Give the position of every leukocyte visible.
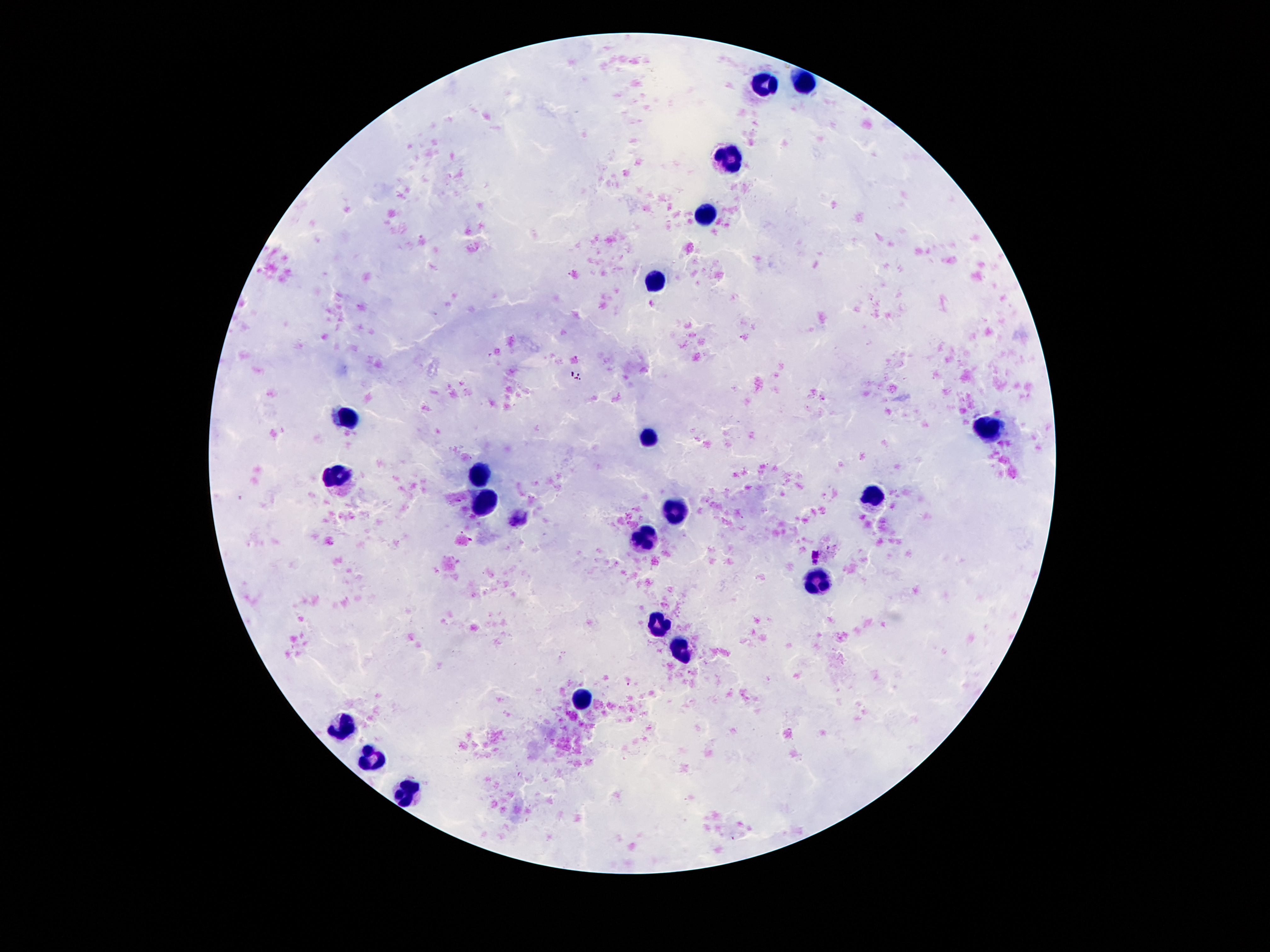
Approximate centers as (x, y) in pixels.
Leukocytes: (805, 81), (761, 87), (727, 159), (705, 215), (657, 279), (349, 417), (990, 430), (650, 439), (480, 472), (336, 476), (873, 495), (486, 503), (674, 515), (645, 539), (816, 581), (657, 625), (685, 652), (584, 696), (343, 725), (369, 760), (407, 793).

field_of_view: one from this slide
magnification: 100x
stain: Giemsa
preparation: thick peripheral-blood smear
capture: smartphone camera through the microscope eyepiece
patient_malaria_status: uninfected
image_size: 1270×952 pixels